Identify the blood parasite species.
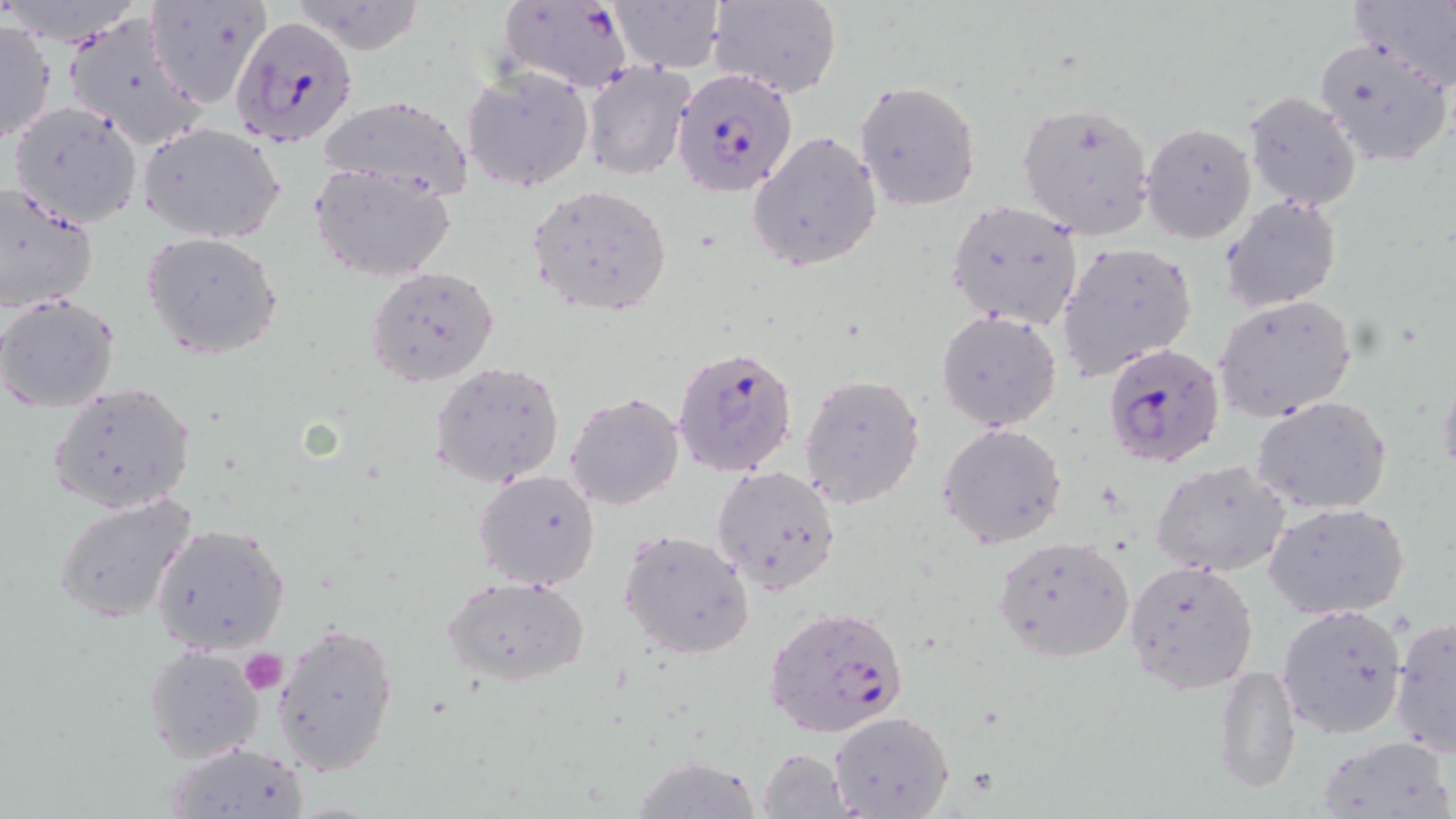
Plasmodium falciparum.

uninfected red blood cell locations = approximate bounding boxes as (x1, y1, x2, y2) in pixels: (710, 0, 842, 99), (1349, 0, 1456, 86), (144, 1, 273, 108), (609, 1, 725, 73), (285, 2, 428, 54), (61, 12, 207, 152), (0, 18, 54, 148), (1313, 36, 1453, 168), (581, 61, 695, 180), (461, 64, 595, 193), (855, 80, 982, 210), (1242, 91, 1361, 211), (316, 94, 472, 201), (6, 101, 141, 231), (1014, 101, 1156, 240), (136, 121, 288, 243), (1140, 122, 1256, 245), (747, 130, 883, 272), (311, 162, 458, 281), (0, 180, 98, 315), (529, 184, 673, 318), (1221, 196, 1341, 312), (945, 199, 1081, 330), (142, 233, 283, 359), (1057, 241, 1198, 380), (364, 266, 499, 387), (0, 293, 120, 411), (1215, 296, 1358, 423), (936, 310, 1061, 431), (429, 360, 565, 487), (1438, 367, 1456, 486), (800, 374, 925, 508), (49, 382, 197, 514), (566, 392, 685, 511), (1251, 396, 1392, 516), (939, 422, 1067, 549), (1150, 459, 1292, 577), (711, 465, 843, 595), (473, 469, 601, 590), (53, 493, 198, 625), (1265, 500, 1410, 620), (151, 523, 290, 654), (617, 529, 753, 661), (993, 534, 1136, 663), (1123, 559, 1260, 694), (444, 574, 591, 686), (1275, 604, 1410, 741), (1390, 616, 1455, 759), (272, 621, 399, 775), (143, 645, 265, 762), (1213, 661, 1300, 796), (829, 711, 956, 819), (1314, 733, 1454, 819), (167, 742, 309, 817), (755, 747, 856, 818), (630, 756, 766, 818)
modality = light microscopy
magnification = 1000x
field of view = one of a larger specimen
image size = 1456×819 pixels
Plasmodium falciparum-infected red blood cell locations = approximate bounding boxes as (x1, y1, x2, y2) in pixels: (497, 0, 633, 92), (228, 13, 356, 149), (671, 68, 799, 197), (1098, 342, 1224, 467), (671, 346, 798, 476), (765, 604, 913, 739)
platelet locations = approximate bounding boxes as (x1, y1, x2, y2) in pixels: (238, 646, 286, 693)
preparation = thin blood film
stain = May-Grünwald-Giemsa